State the preparation type.
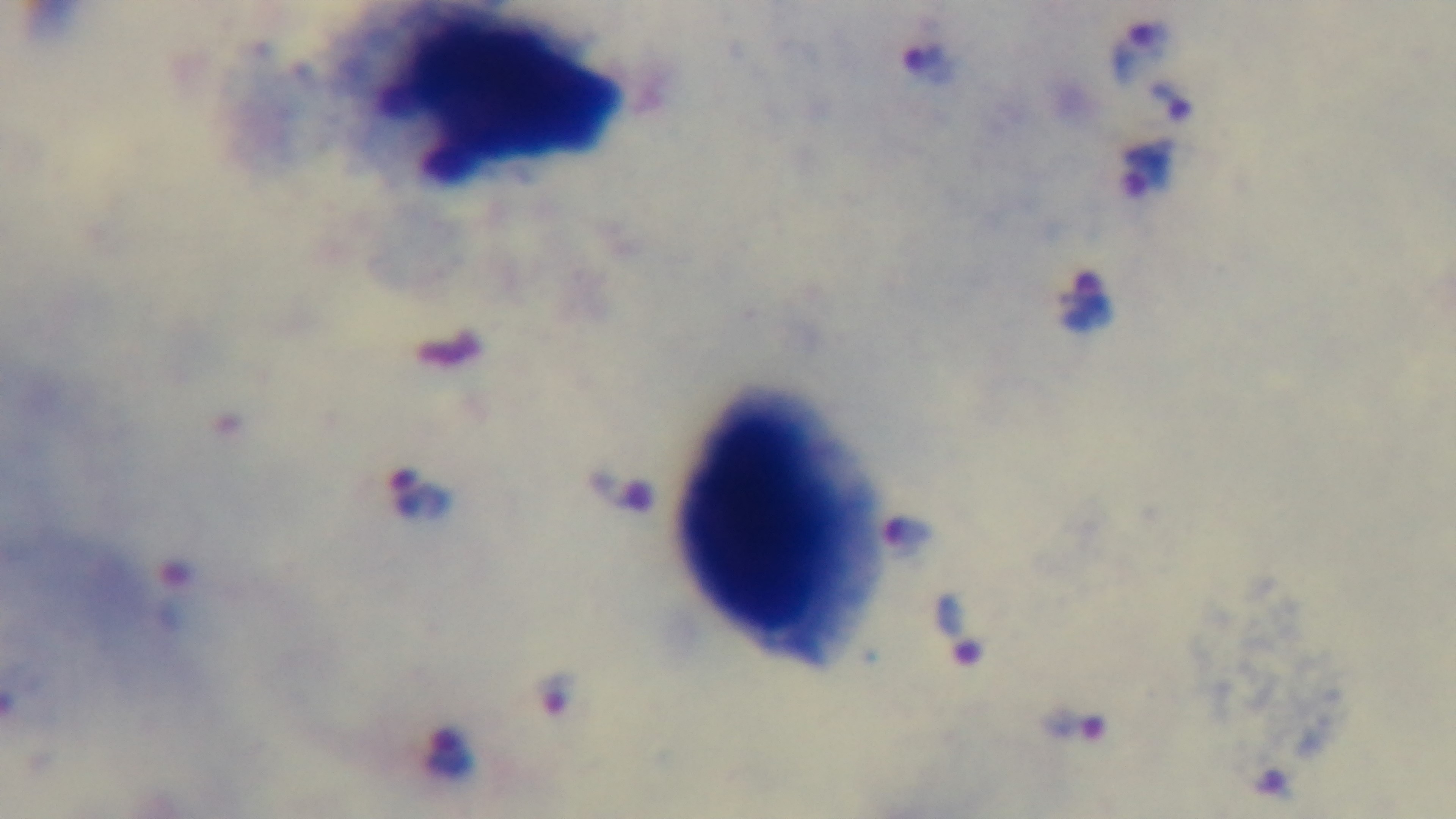
It is a thick blood film.

Summary:
  - Malaria status: positive
  - Modality: light microscopy
  - Objective: 100x oil immersion
  - Stain: Giemsa
  - Field of view: one from the slide
  - Capture: mounted 4K digital camera